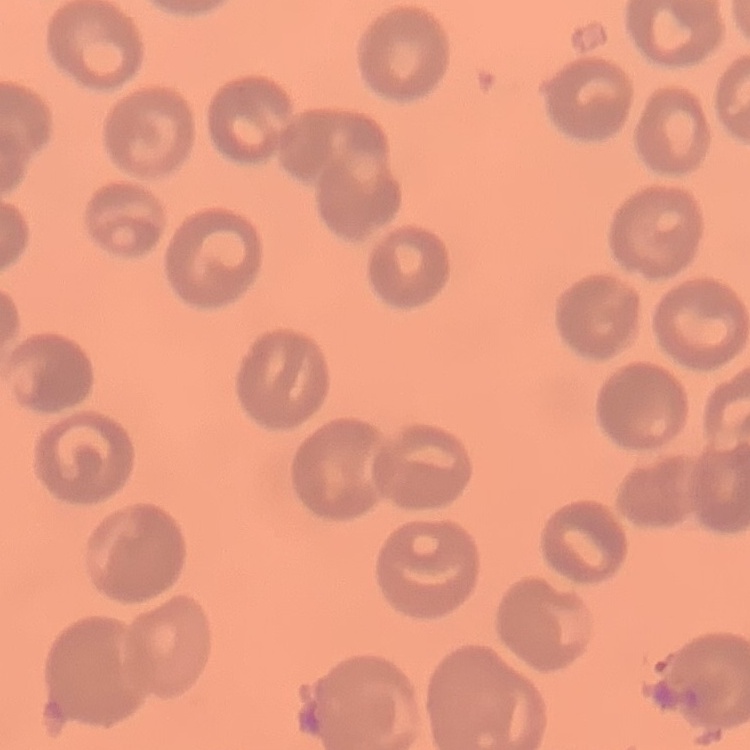
red_blood_cell_morphology: no rouleaux formation
image_type: square crop of a larger photomicrograph
preparation: thin blood smear
stain: Field's or Giemsa